Locate every Plasmodium parasite.
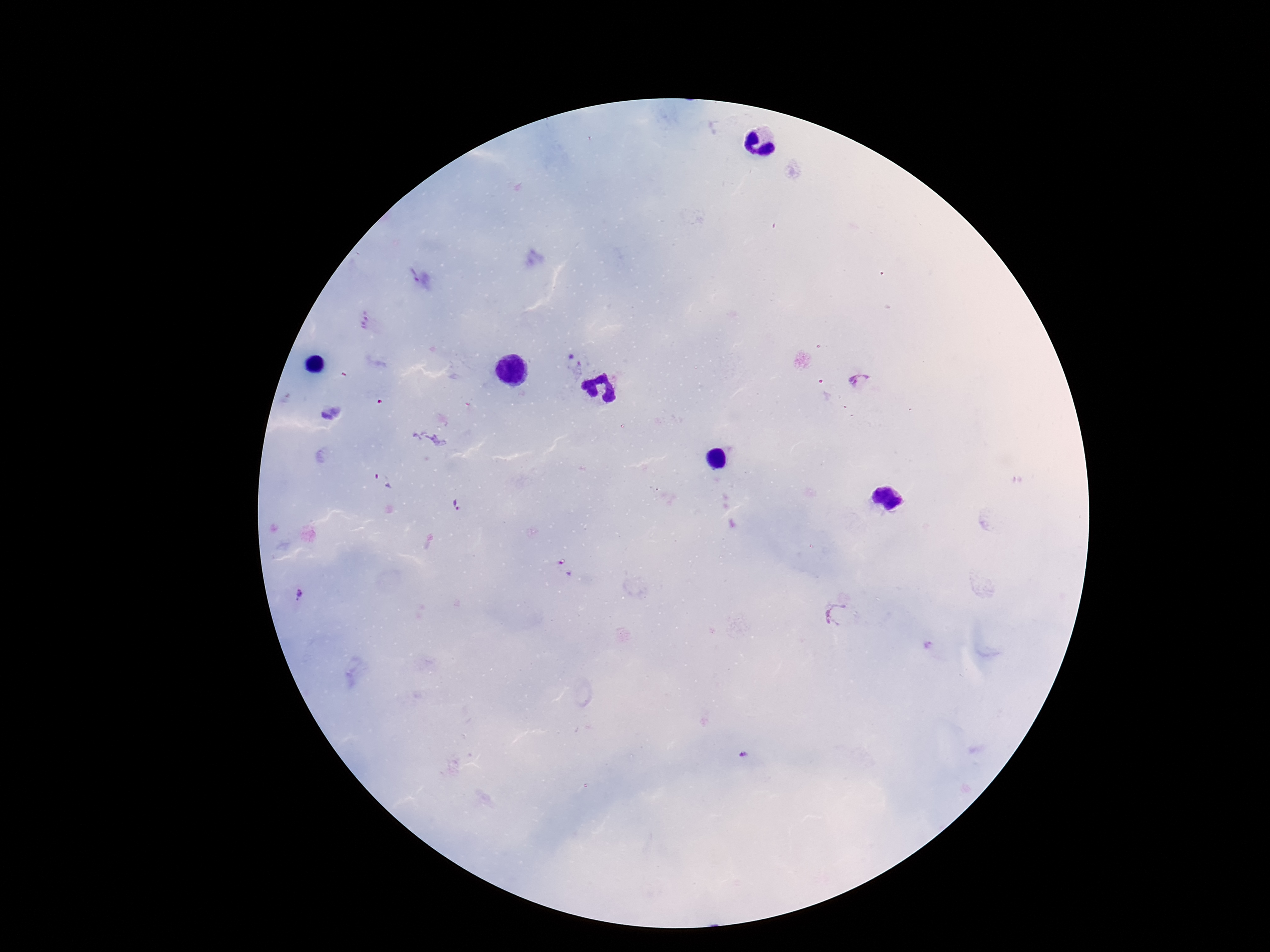
Approximate centers as (x, y) in pixels.
Plasmodium parasites: (413, 275), (575, 365), (858, 381), (383, 483), (455, 507), (300, 595), (836, 613), (744, 756).

capture: smartphone camera through the microscope eyepiece
magnification: 100x
field_of_view: single
preparation: thick blood film
stain: Giemsa
patient_malaria_status: infected
image_size: 1270×952 pixels